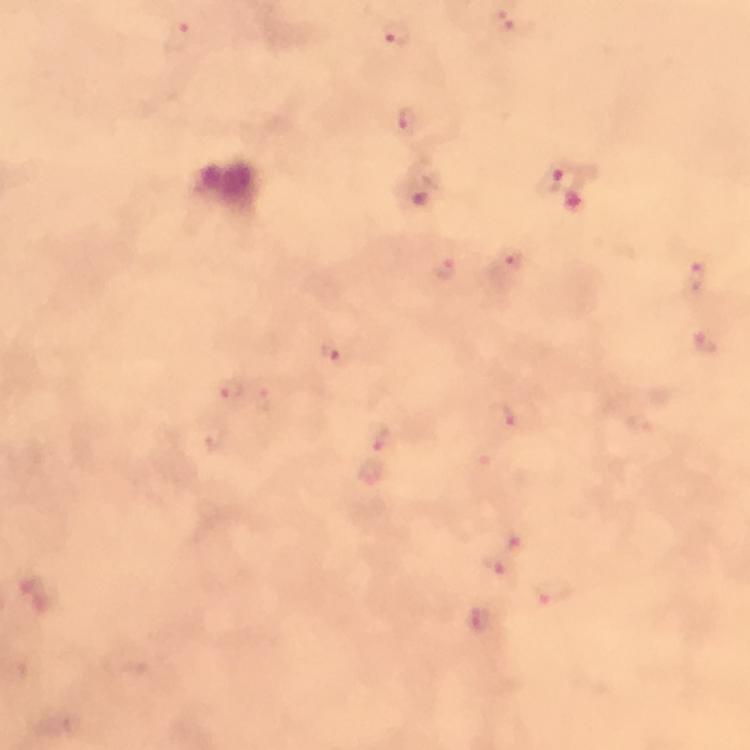
magnification = 100x
capture = smartphone camera through the microscope
immersion oil = used
preparation = thick blood smear
stain = Giemsa
cropped from = a single field of view
context = from a malaria diagnostic workup
malaria parasite locations = approximate object centers, in pixels from the top-left corner: (x=504, y=20), (x=396, y=34), (x=178, y=37), (x=404, y=120), (x=549, y=175), (x=573, y=200), (x=511, y=260), (x=441, y=266), (x=696, y=276), (x=706, y=342), (x=331, y=353), (x=231, y=390), (x=262, y=398), (x=501, y=416), (x=378, y=434), (x=514, y=538), (x=496, y=565), (x=553, y=592)
image size = 750×750 pixels